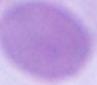
1000x magnification. Micrograph. A red blood cell is seen.